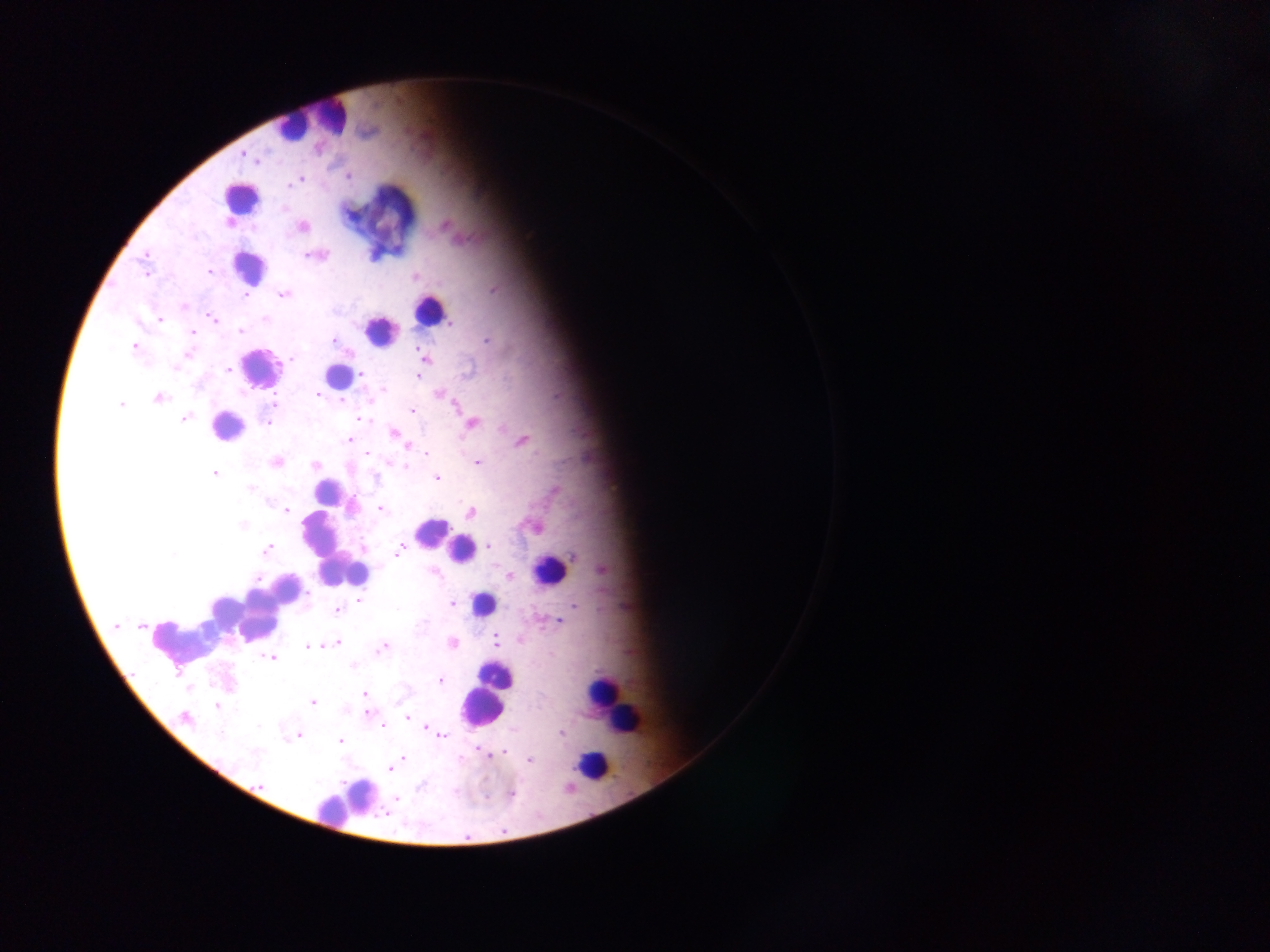
country = Ghana
leukocyte locations = approximate centers as (x, y) in pixels: (333, 116), (294, 125), (240, 198), (248, 267), (429, 311), (379, 331), (259, 368), (340, 377), (225, 426), (327, 489), (432, 532), (327, 547), (461, 550), (549, 569), (268, 604), (483, 604), (196, 629), (496, 676), (603, 693), (483, 706), (614, 708), (623, 720), (589, 766), (356, 796)
image size = 1270×952 pixels
preparation = thick blood smear
capture = mobile-phone photograph through a microscope
field of view = single
malaria parasite locations = approximate centers as (x, y) in pixels: (244, 155), (257, 160), (348, 176), (301, 180), (445, 226), (304, 227), (309, 255), (146, 256), (145, 271), (209, 272), (414, 277), (493, 290), (284, 294), (246, 296), (212, 317), (266, 318), (160, 319), (452, 323), (240, 331), (193, 332), (487, 340), (334, 341), (133, 347), (418, 350), (186, 355), (291, 358), (426, 359), (228, 370), (363, 374), (418, 376), (383, 389), (439, 393), (318, 395), (159, 398), (343, 401), (273, 403), (121, 404), (455, 407), (412, 411), (185, 419), (364, 420), (268, 423), (472, 423), (394, 432), (350, 440), (522, 440), (408, 448), (426, 453), (367, 454), (277, 462), (389, 463), (478, 463), (315, 465), (404, 466), (214, 474), (436, 478), (250, 489), (554, 491), (381, 509), (287, 510), (471, 513), (243, 524), (489, 546), (364, 547), (267, 549), (398, 552), (572, 556), (602, 570), (509, 576), (360, 601), (453, 604), (575, 606), (336, 611), (558, 621), (117, 626), (141, 626), (495, 640), (337, 642), (452, 643), (308, 646), (383, 647), (270, 658), (352, 666), (440, 681), (365, 694), (313, 703), (217, 706), (406, 717), (184, 718), (384, 727), (425, 728), (433, 732), (561, 732), (220, 735), (442, 735), (298, 736), (340, 741), (485, 752), (505, 752), (403, 758), (529, 761), (390, 768), (260, 785), (419, 786), (512, 793), (396, 798)